Locate every Plasmodium parasite.
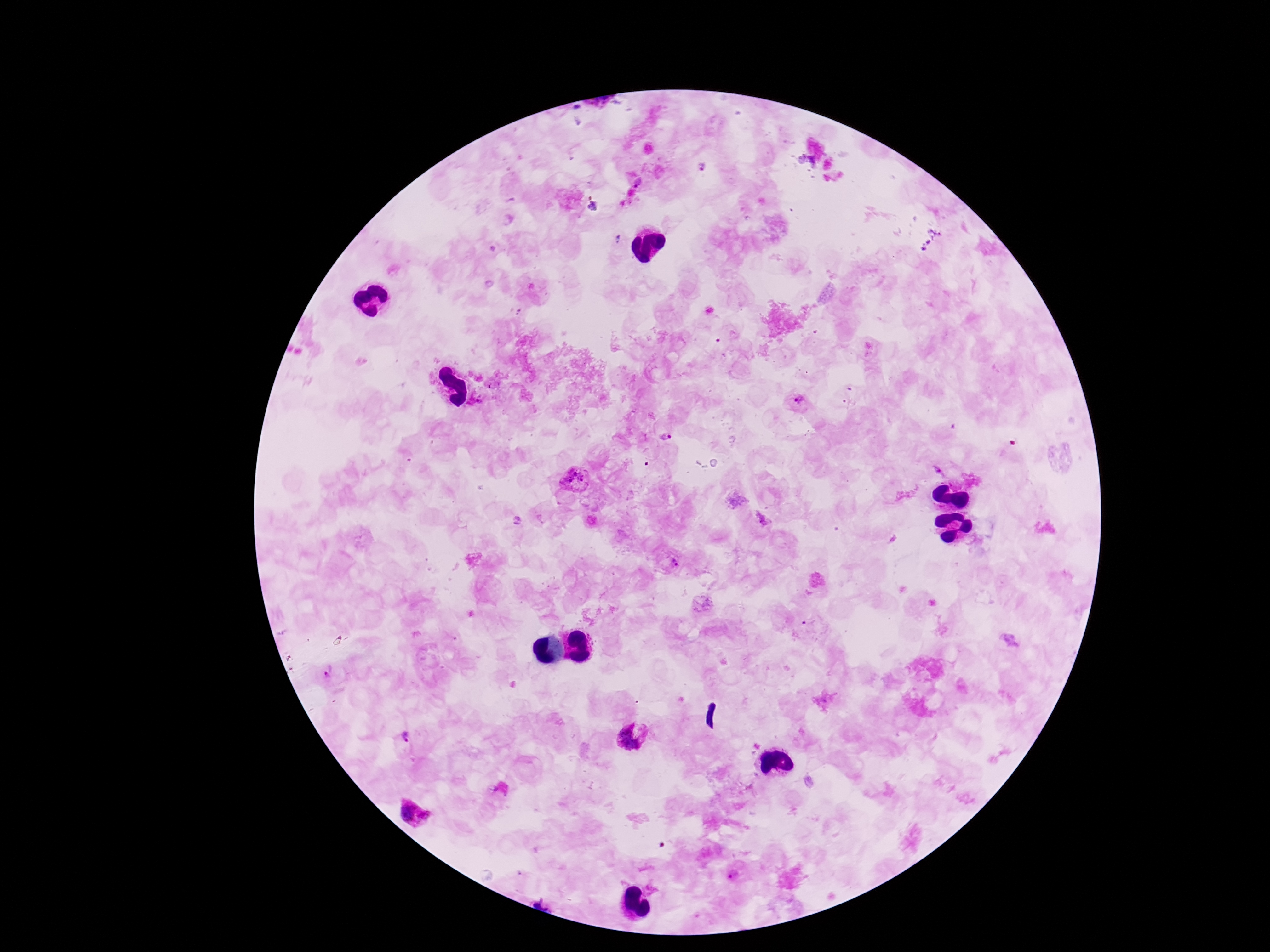
Approximate centers as [x, y] in pixels.
Plasmodium parasites: [701, 167], [638, 183], [593, 207], [619, 240], [798, 402], [666, 437], [940, 471], [575, 479], [675, 561], [329, 670], [631, 738], [415, 815].

stain = Giemsa
magnification = 100x
field of view = single
patient malaria status = positive
preparation = thick blood smear
image size = 1270×952 pixels
capture = smartphone camera through the microscope eyepiece